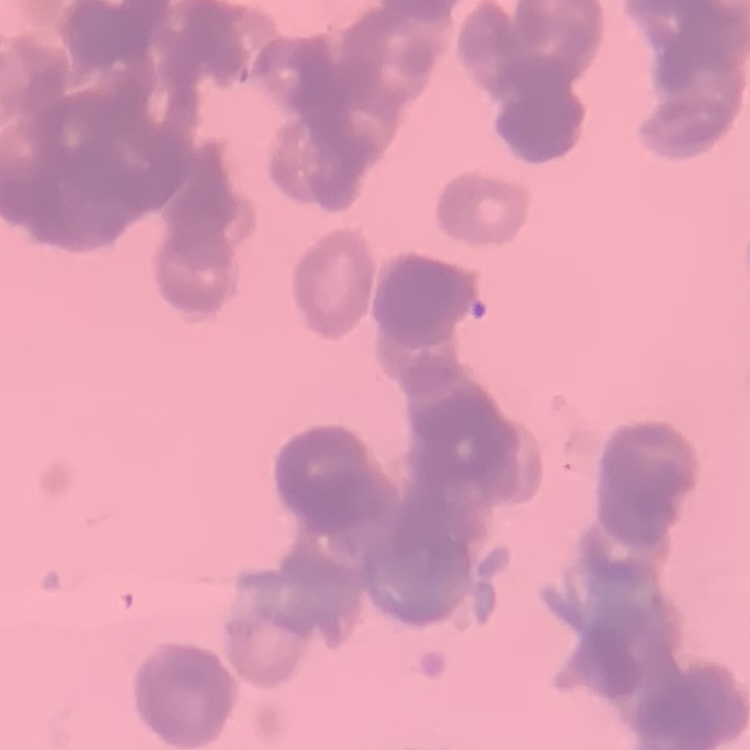

Summary:
  - Red blood cell morphology: rouleaux formation
  - Preparation: thin peripheral smear
  - Image type: square crop of a larger photomicrograph
  - Stain: Field's or Giemsa